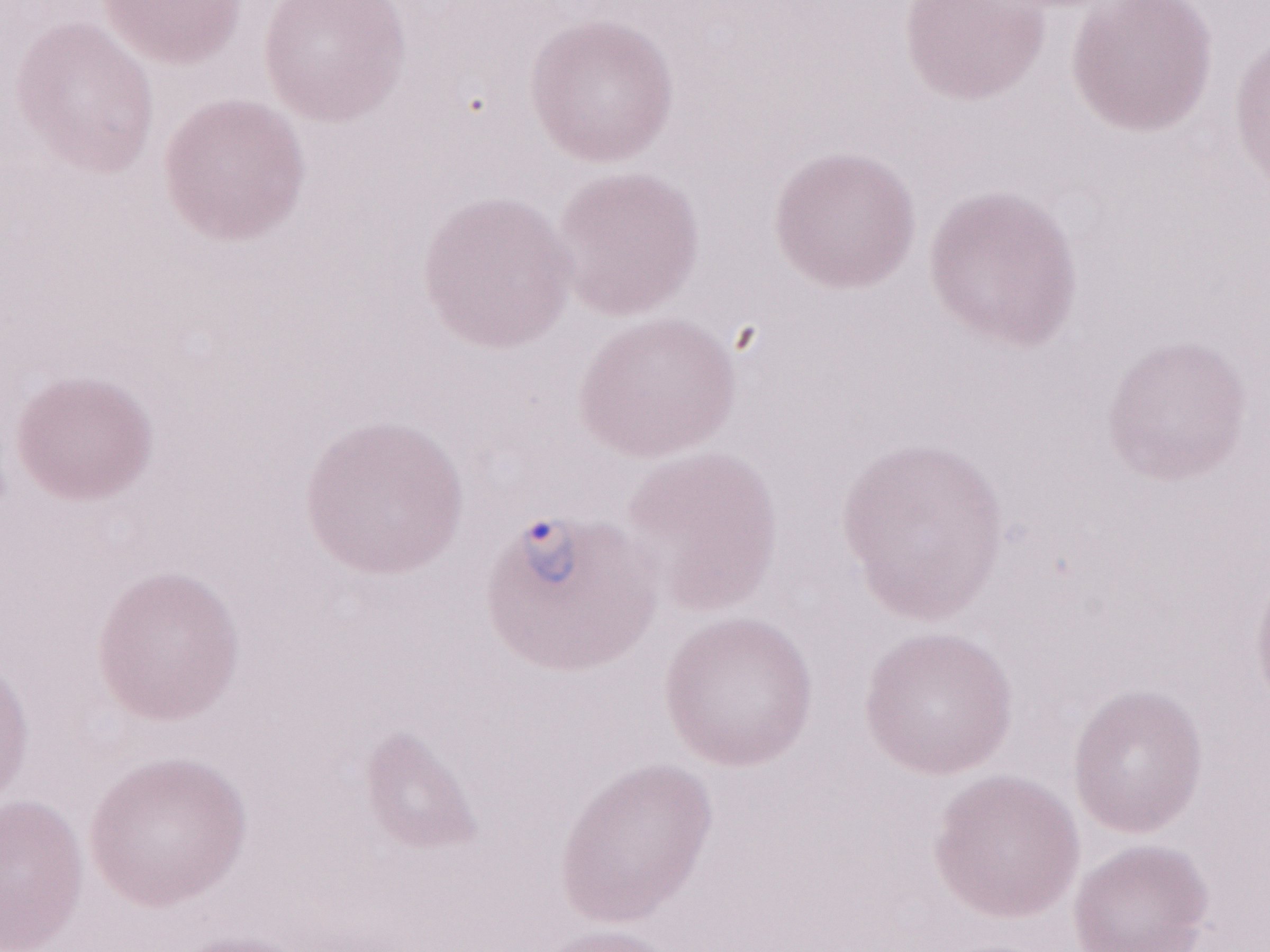

Image is 1270×952 pixels. Malaria diagnosis (patient-level): positive. May-Grünwald-Giemsa (MGG) stain. Single field of view. 1,000x magnification. Thin blood film. Olympus BX43 microscope, Olympus DP73 camera.